Identify the parasite.
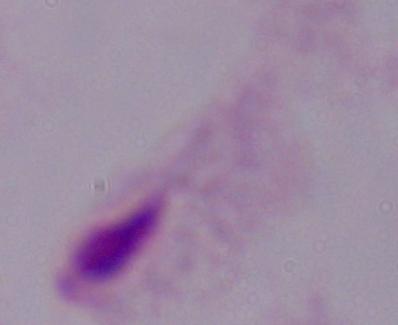

This is a trichomonad.

Micrograph. 1000x magnification.